Report the malaria status of this cell.
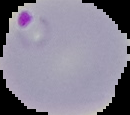

Parasitized.

{
  "preparation": "thin blood smear",
  "image_type": "cell region segmented out of the field of view; surrounding area masked to black",
  "image_size": "130×115 pixels"
}